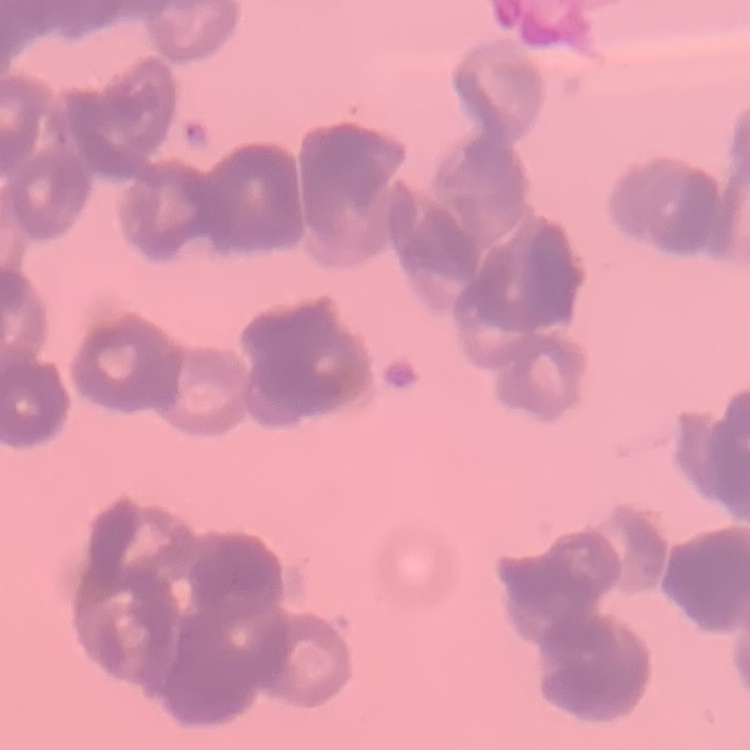
{
  "erythrocyte_morphology": "rouleaux formation",
  "stain": "Field's or Giemsa",
  "image_type": "one tile cut from a larger photomicrograph",
  "preparation": "thin blood smear"
}